Classify this cell by malaria status.
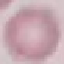

It is uninfected.

Giemsa stain. Thin blood film. Automatically extracted cell patch, resized to 64 × 64 pixels. Photographed with a smartphone camera at the microscope eyepiece.